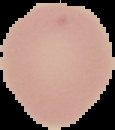
Cell region segmented out of the field of view; the surrounding area is masked to black. Malaria status: uninfected. From a thin blood film. Image is 115×130 pixels.